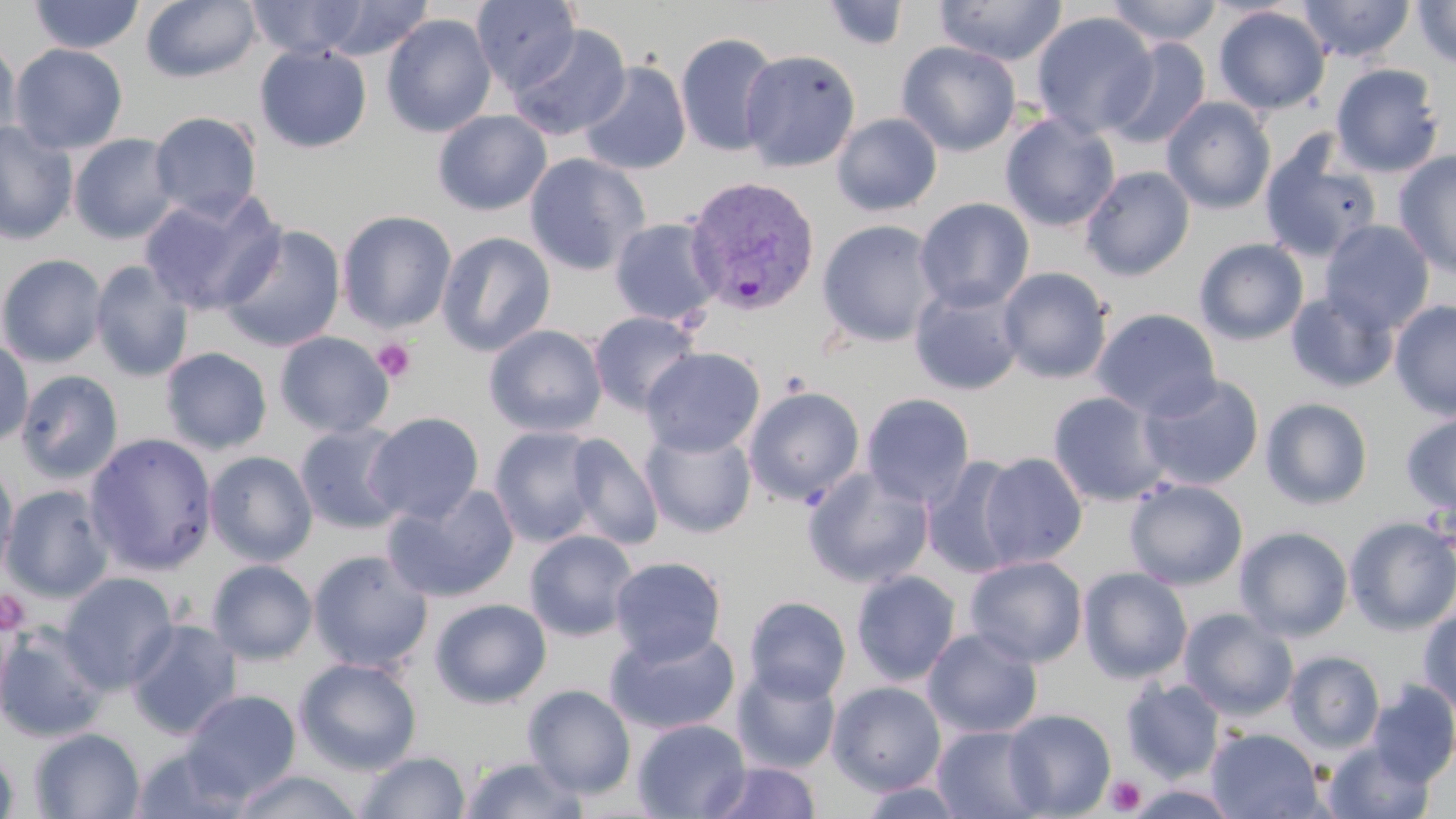
Approximate bounding boxes as [x1, y1, x2, y2] in pixels. Uninfected red blood cell locations: [27, 0, 145, 54], [141, 0, 261, 83], [248, 0, 368, 59], [318, 0, 434, 60], [470, 0, 581, 93], [935, 0, 1067, 66], [1105, 0, 1223, 46], [1298, 0, 1415, 62], [1412, 0, 1456, 69], [821, 1, 910, 52], [1213, 5, 1331, 115], [1030, 11, 1159, 139], [381, 14, 497, 138], [507, 24, 632, 141], [675, 32, 781, 157], [0, 37, 22, 152], [1104, 38, 1212, 151], [896, 41, 1022, 156], [9, 43, 128, 154], [255, 43, 372, 153], [740, 48, 861, 172], [577, 61, 692, 176], [1330, 63, 1445, 177], [1162, 97, 1276, 214], [432, 110, 552, 216], [149, 111, 263, 220], [831, 113, 942, 216], [1000, 113, 1120, 232], [0, 121, 78, 245], [68, 133, 179, 244], [1258, 134, 1382, 263], [1394, 150, 1456, 278], [524, 153, 650, 276], [1080, 166, 1195, 281], [138, 190, 285, 315], [914, 197, 1035, 312], [337, 210, 457, 333], [610, 216, 724, 326], [816, 219, 941, 347], [1320, 220, 1434, 334], [217, 223, 347, 353], [436, 231, 557, 357], [1194, 238, 1309, 345], [0, 253, 107, 367], [90, 260, 194, 382], [997, 266, 1113, 384], [909, 281, 1025, 395], [1285, 290, 1399, 393], [1390, 299, 1456, 419], [1091, 308, 1222, 420], [588, 311, 702, 415], [484, 324, 608, 437], [274, 331, 394, 438], [0, 338, 34, 447], [160, 347, 272, 455], [641, 347, 765, 457], [16, 369, 124, 484], [1138, 374, 1264, 490], [743, 385, 866, 507], [1046, 390, 1170, 507], [860, 393, 976, 508], [1260, 397, 1373, 510], [1401, 411, 1456, 517], [363, 412, 485, 524], [295, 422, 408, 534], [489, 426, 602, 547], [640, 426, 757, 539], [83, 432, 218, 575], [565, 433, 663, 550], [204, 450, 318, 566], [977, 452, 1088, 568], [922, 456, 1025, 578], [0, 466, 20, 578], [802, 467, 934, 588], [1123, 478, 1248, 590], [383, 483, 520, 603], [1, 485, 115, 602], [1344, 517, 1456, 634], [1234, 526, 1354, 641], [523, 530, 639, 641], [307, 549, 433, 672], [965, 555, 1088, 667], [609, 556, 727, 665], [207, 560, 318, 664], [1078, 567, 1193, 684], [851, 570, 961, 686], [58, 571, 179, 693], [744, 596, 851, 703], [429, 598, 552, 708], [1418, 605, 1456, 716], [1179, 609, 1298, 720], [126, 619, 242, 738], [0, 626, 110, 743], [605, 627, 740, 735], [922, 627, 1043, 738], [1284, 651, 1385, 754], [294, 657, 422, 775], [732, 665, 841, 773], [1121, 678, 1226, 783], [827, 681, 947, 795], [1368, 681, 1456, 786], [522, 684, 636, 798], [183, 690, 301, 801], [1003, 709, 1116, 817], [632, 718, 751, 818], [932, 723, 1050, 818], [29, 727, 145, 818], [1206, 727, 1325, 818], [1324, 740, 1434, 818], [0, 745, 19, 818], [131, 745, 254, 819], [354, 751, 471, 818], [459, 755, 588, 818], [704, 760, 822, 819], [230, 769, 364, 819], [857, 781, 970, 818]. Platelet locations: [372, 338, 416, 384], [0, 589, 31, 636], [1105, 775, 1147, 815]. Plasmodium vivax-infected red blood cell locations: [684, 175, 821, 316]. Slide-level diagnosis: Plasmodium vivax. May-Grünwald-Giemsa-stained preparation. One field of a larger specimen. Thin blood smear. 1000x magnification. Image is 1456×819 pixels. Light microscopy.